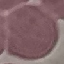

Summary:
  - Result: no malaria parasites detected
  - Capture: smartphone camera at the microscope eyepiece
  - Stain: Giemsa
  - Preparation: thin blood smear
  - Image type: cell patch, automatically extracted from a larger field of view and resized to 64 × 64 pixels